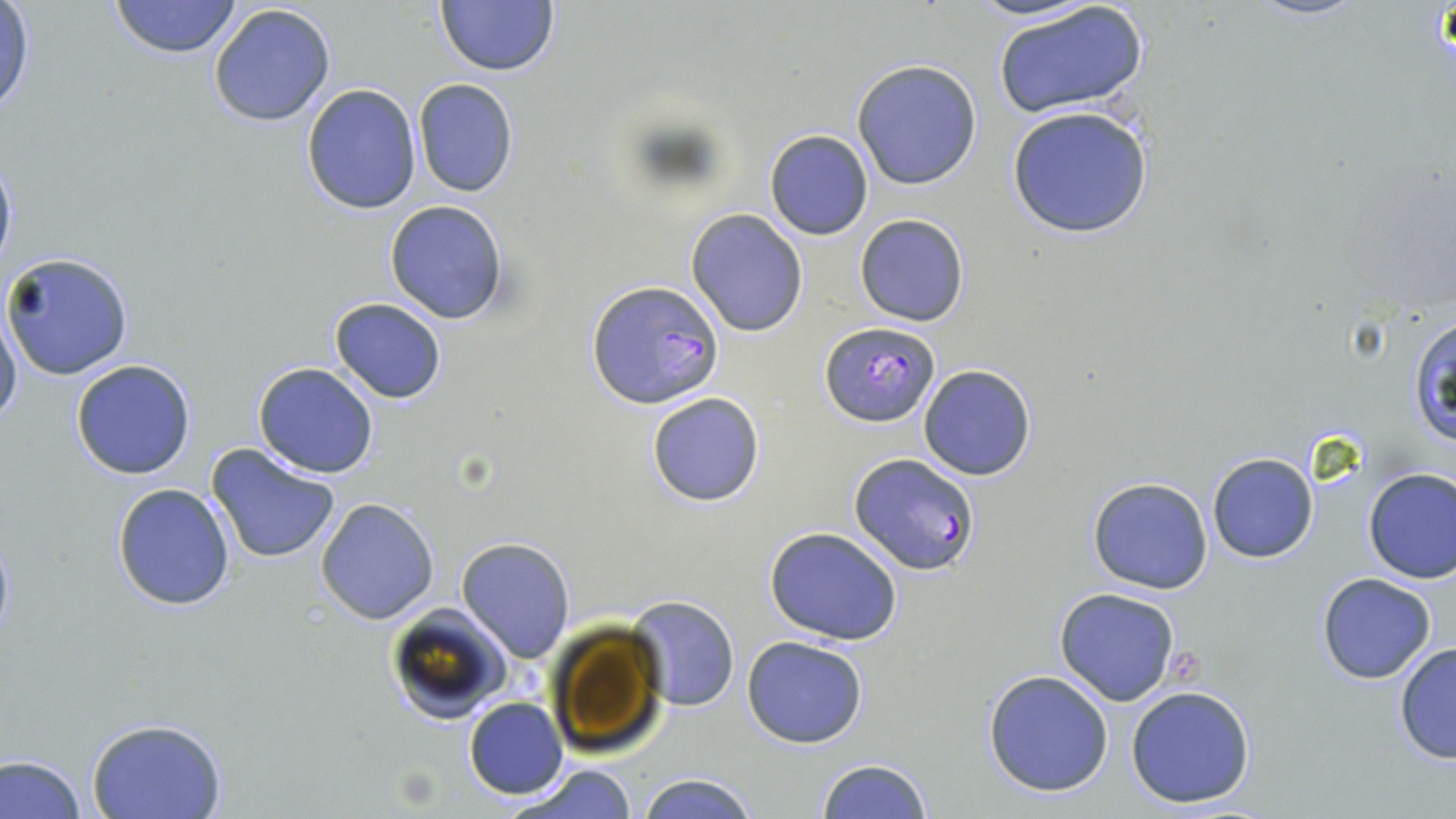
slide_level_diagnosis: Plasmodium falciparum
preparation: thin blood smear
plasmodium_falciparum_infected_red_blood_cell_locations: 'approximate bounding boxes as [x1, y1, x2, y2] in pixels: [586, 278, 723, 410], [820, 322, 940, 428], [850, 450, 979, 574]'
uninfected_red_blood_cell_locations: 'approximate bounding boxes as [x1, y1, x2, y2] in pixels: [110, 0, 242, 59], [435, 0, 560, 78], [963, 0, 1101, 25], [1247, 0, 1367, 22], [991, 2, 1147, 119], [0, 3, 35, 119], [208, 3, 337, 128], [852, 58, 982, 190], [412, 79, 519, 199], [300, 83, 421, 215], [1006, 107, 1151, 239], [764, 130, 874, 240], [0, 148, 17, 281], [384, 200, 511, 323], [685, 208, 810, 337], [855, 213, 969, 326], [2, 251, 134, 380], [329, 298, 447, 404], [1, 308, 22, 431], [70, 359, 197, 480], [917, 363, 1037, 482], [253, 364, 379, 478], [646, 391, 765, 507], [206, 442, 343, 565], [1206, 452, 1318, 564], [1362, 467, 1456, 584], [1087, 476, 1214, 594], [111, 483, 236, 611], [315, 497, 440, 624], [764, 527, 905, 645], [457, 537, 575, 661], [1317, 572, 1437, 684], [1054, 587, 1182, 707], [627, 595, 740, 711], [385, 603, 512, 725], [742, 636, 869, 749], [1393, 641, 1456, 764], [982, 670, 1114, 796], [1125, 685, 1258, 810], [463, 698, 567, 799], [85, 716, 226, 819], [0, 752, 87, 818], [815, 758, 933, 819], [503, 762, 642, 819], [636, 772, 760, 818]'
magnification: 1000x
image_size: 1456×819 pixels
stain: May-Grünwald-Giemsa
field_of_view: single
modality: light microscopy